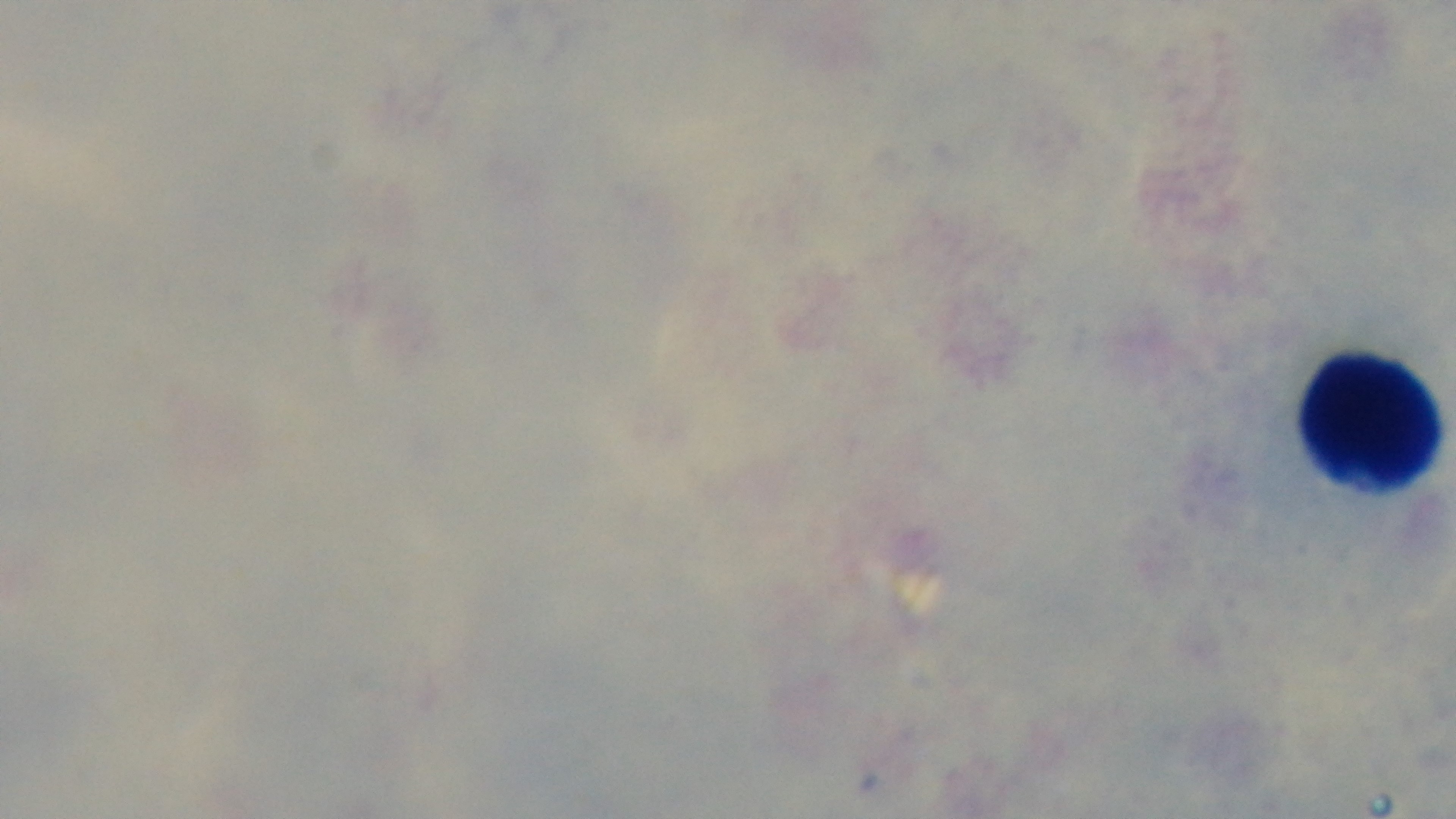

malaria status = negative
stain = Giemsa
field of view = one from the slide
objective = 100x oil immersion
modality = light microscopy
capture = mounted 4K digital camera
preparation = thick smear